Locate every Plasmodium parasite.
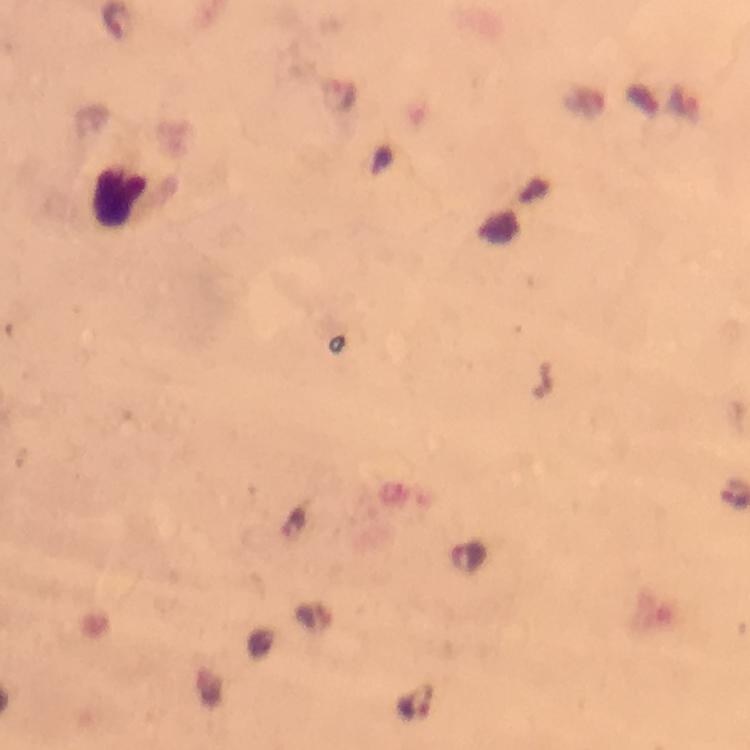
Approximate centers as [x, y] in pixels.
Plasmodium parasites: [414, 702].

immersion_oil: applied
stain: Giemsa
magnification: 100x
preparation: thick smear
cropped_from: one field of view
leukocyte_locations: 'approximate centers as [x, y] in pixels: [121, 197], [515, 212]'
image_size: 750×750 pixels
capture: smartphone photograph through a microscope
context: from a malaria diagnostic workup